Locate every Plasmodium parasite.
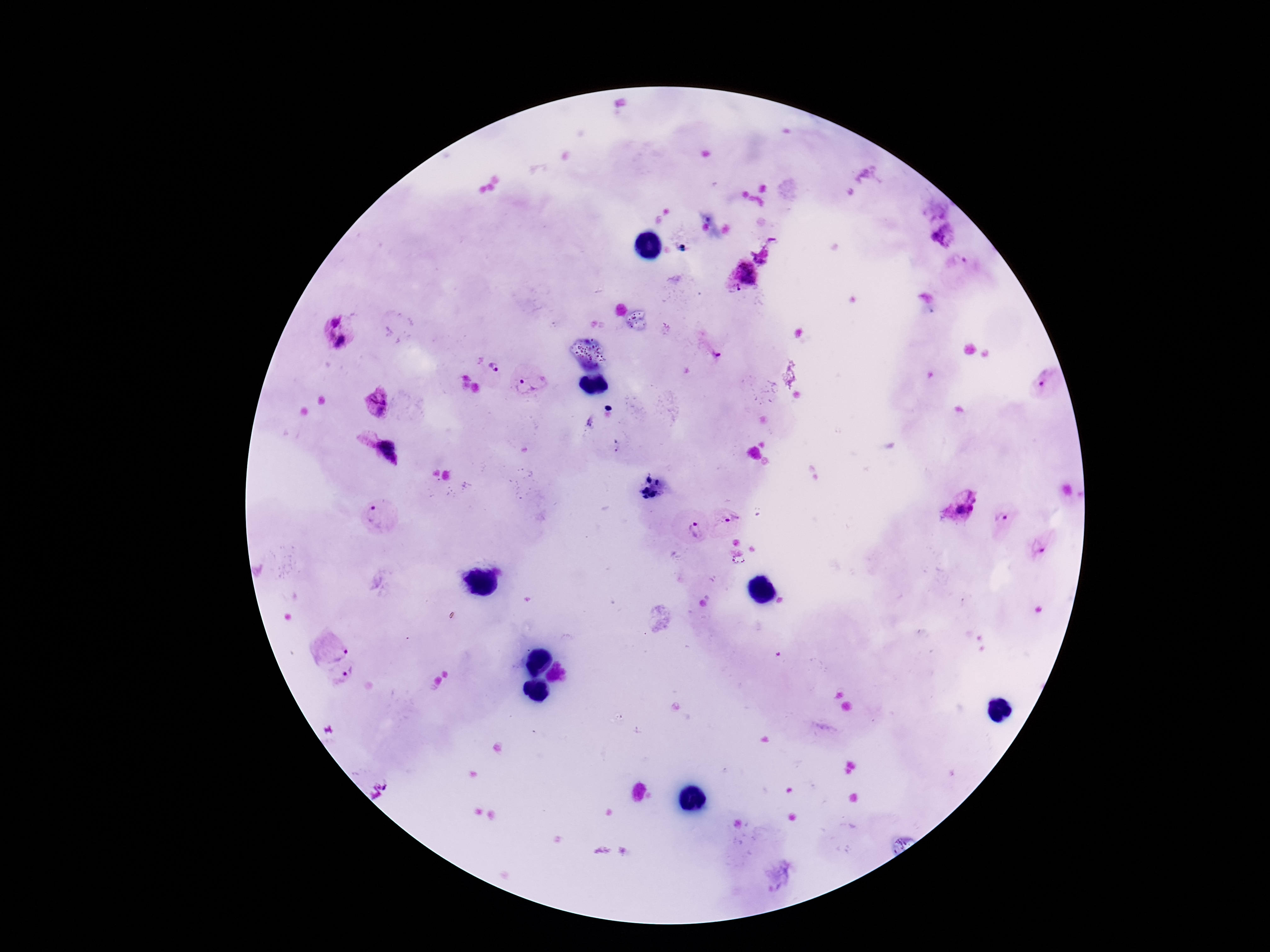
Approximate object centers, in pixels from the top-left corner.
Plasmodium parasites: (x=943, y=234), (x=742, y=276), (x=334, y=320), (x=341, y=344), (x=713, y=354), (x=494, y=368), (x=1043, y=384), (x=531, y=385), (x=377, y=403), (x=376, y=453), (x=959, y=506), (x=377, y=515), (x=1003, y=516), (x=729, y=520), (x=694, y=530), (x=1038, y=547), (x=333, y=650), (x=347, y=675).

Summary:
  - Stain: Giemsa
  - Magnification: 100x
  - Field of view: one from this slide
  - Preparation: thick blood smear
  - Patient malaria status: infected
  - Image size: 1270×952 pixels
  - Capture: smartphone camera through the microscope eyepiece